Assess this cell for malaria.
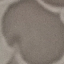
It is uninfected.

Thin blood film. Giemsa-stained preparation. Acquired by smartphone through the microscope eyepiece. Automatically extracted cell patch, resized to 64 × 64 pixels.